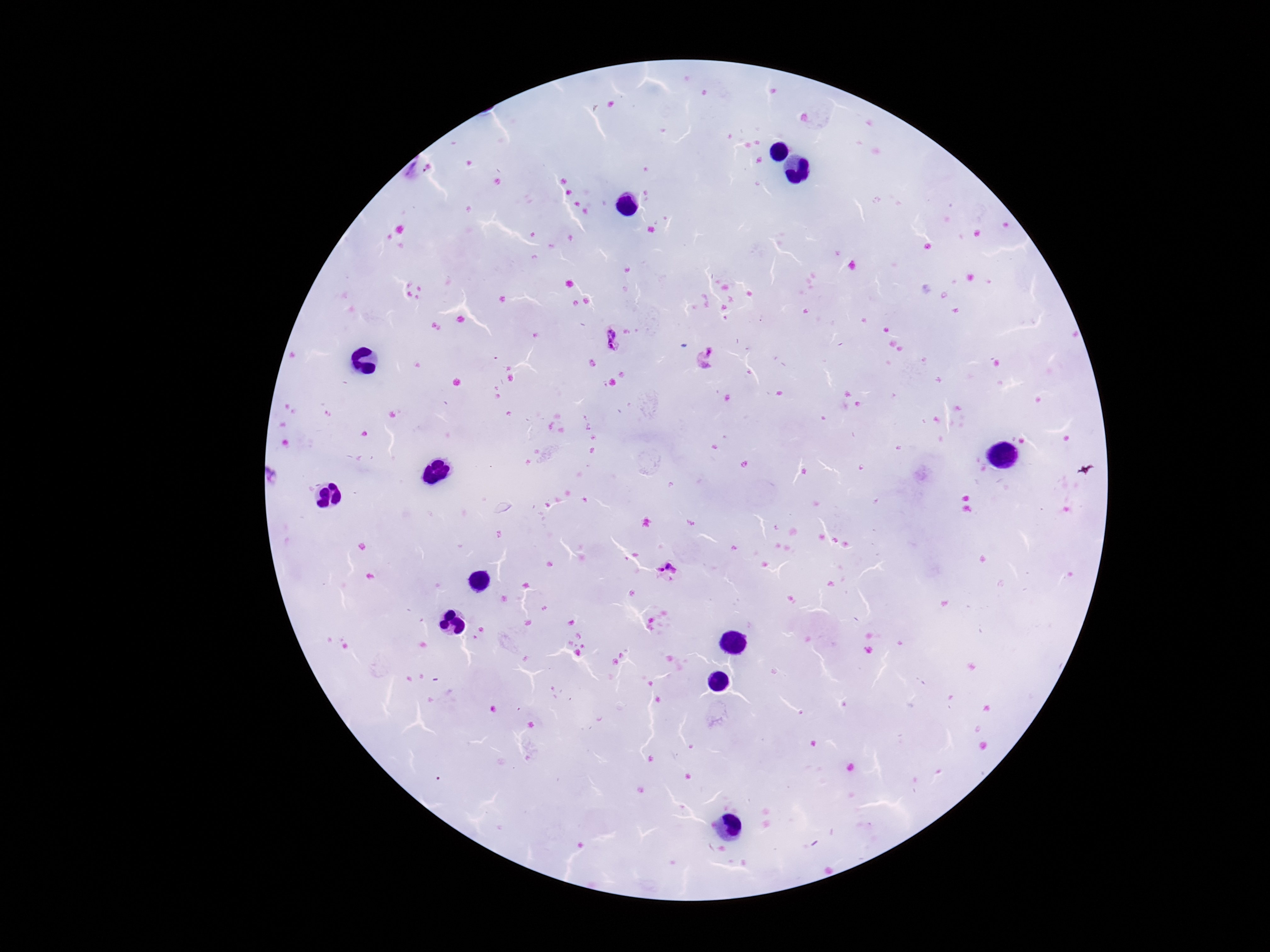
Approximate centers as (x, y) in pixels. Plasmodium parasite locations: (424, 169), (611, 339), (708, 357), (665, 572). Smartphone photograph taken through the microscope eyepiece. 100x magnification. Image is 1270×952 pixels. Single field of view. Thick blood smear. Patient malaria status: infected. Giemsa stain.